Classify this cell by malaria status.
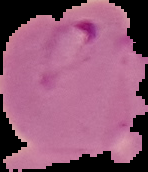
It is parasitized.

Segmented cell region on a black background. From a thin blood smear. Image is 148×172 pixels.